Identify the blood parasite species.
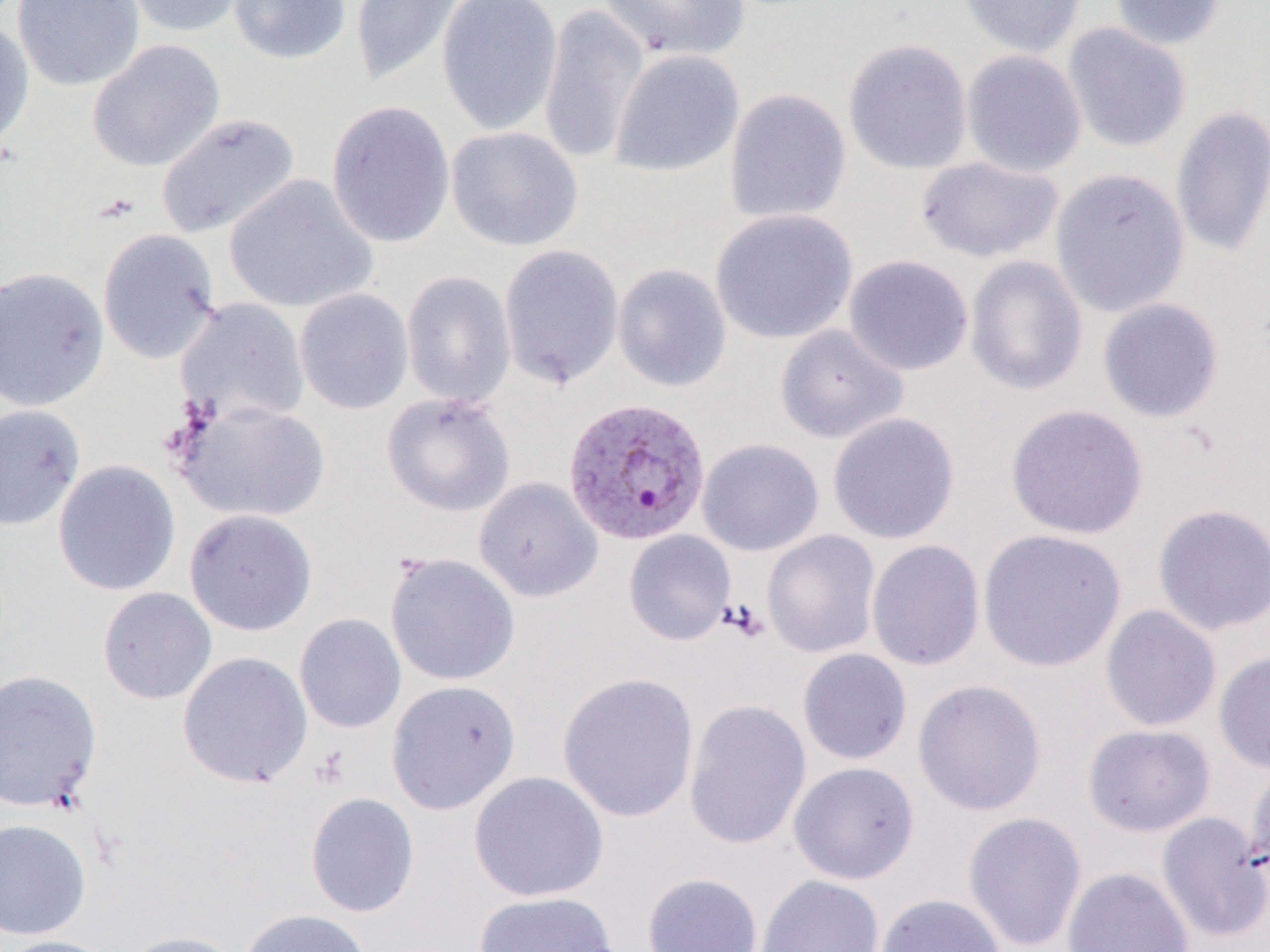
Plasmodium vivax.

Summary:
  - Coordinate format: approximate bounding boxes as [x1, y1, x2, y2] in pixels
  - Uninfected red blood cell locations: [11, 0, 145, 91], [119, 0, 250, 38], [227, 0, 352, 65], [350, 0, 467, 86], [437, 0, 563, 136], [598, 0, 750, 61], [956, 0, 1086, 59], [1110, 0, 1226, 51], [537, 3, 649, 166], [0, 18, 35, 152], [1062, 23, 1191, 153], [843, 38, 973, 175], [86, 39, 225, 173], [610, 49, 744, 177], [961, 50, 1087, 178], [724, 87, 852, 225], [325, 100, 456, 249], [1170, 105, 1270, 258], [155, 112, 301, 240], [446, 126, 583, 252], [915, 156, 1064, 263], [1050, 168, 1190, 318], [224, 174, 378, 314], [710, 208, 858, 344], [97, 228, 221, 365], [499, 245, 624, 390], [843, 254, 974, 377], [965, 255, 1088, 396], [612, 264, 732, 392], [0, 266, 110, 412], [401, 270, 516, 409], [293, 288, 414, 415], [175, 297, 310, 427], [1097, 298, 1225, 423], [775, 324, 908, 444], [381, 392, 515, 517], [173, 399, 331, 523], [0, 403, 87, 531], [1005, 403, 1148, 540], [827, 412, 960, 545], [697, 438, 824, 557], [52, 460, 181, 596], [474, 477, 603, 602], [1152, 503, 1270, 636], [183, 508, 318, 636], [977, 528, 1126, 672], [762, 529, 881, 658], [623, 530, 736, 646], [866, 539, 985, 671], [384, 552, 520, 686], [97, 587, 217, 705], [1100, 605, 1222, 732], [294, 613, 406, 733], [797, 648, 912, 765], [177, 651, 313, 788], [1213, 652, 1270, 774], [0, 669, 102, 812], [556, 671, 700, 824], [386, 679, 521, 815], [912, 679, 1047, 816], [683, 699, 812, 851], [1082, 723, 1215, 837], [788, 761, 919, 884], [1245, 761, 1270, 880], [469, 770, 609, 902], [305, 792, 420, 917], [962, 811, 1087, 951], [1156, 812, 1270, 944], [0, 818, 91, 940], [1062, 866, 1193, 952], [642, 872, 763, 952], [755, 874, 885, 952], [473, 890, 620, 952], [875, 893, 1006, 952], [238, 909, 373, 952], [118, 930, 248, 952], [0, 935, 118, 952]
  - Platelet locations: [721, 599, 768, 642]
  - Plasmodium vivax-infected red blood cell locations: [562, 397, 711, 547]
  - Preparation: thin blood smear
  - Modality: light microscopy
  - Magnification: 1000x
  - Field of view: single
  - Image size: 1270×952 pixels